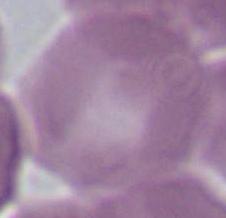
magnification: 1000x
modality: photomicrograph
identification: red blood cell